Report the malaria status of this cell.
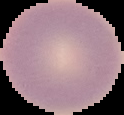
Uninfected.

Summary:
  - Image size: 124×115 pixels
  - Image type: segmented cell region with the area outside set to black
  - Preparation: thin blood smear